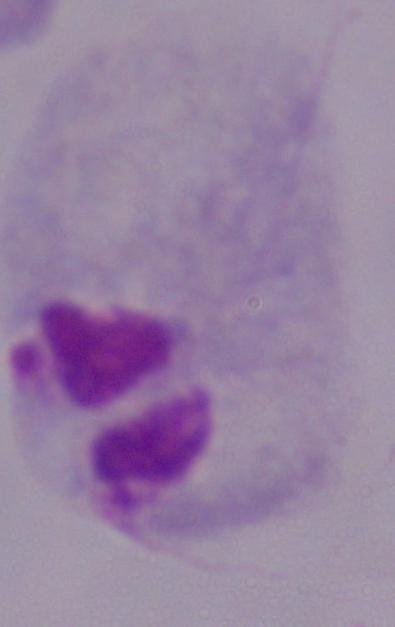

magnification = 1000x
modality = photomicrograph
identification = trichomonad